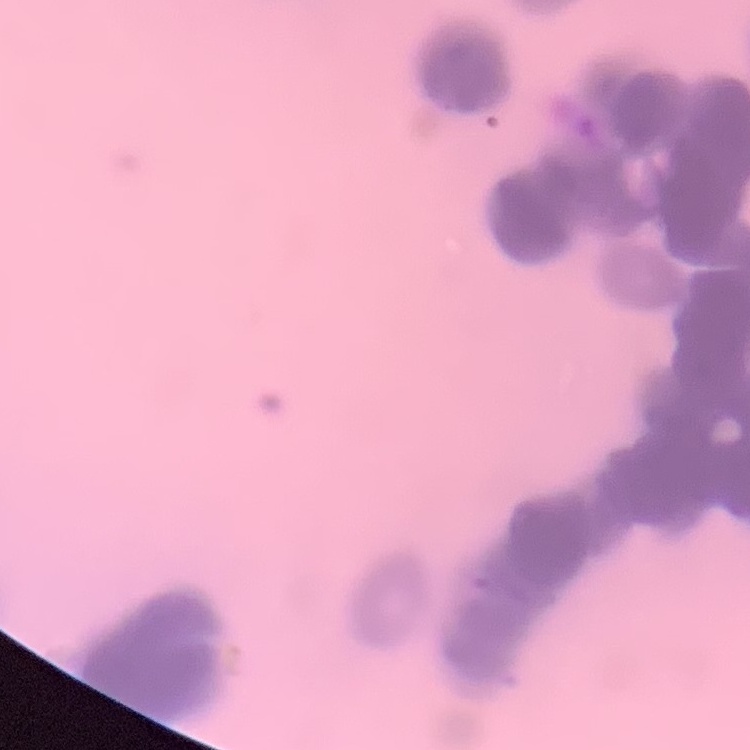

The erythrocytes exhibit rouleaux formation. Thin blood film. Field's or Giemsa stain. Square crop of a larger photomicrograph.